Assess the morphology of the erythrocytes.
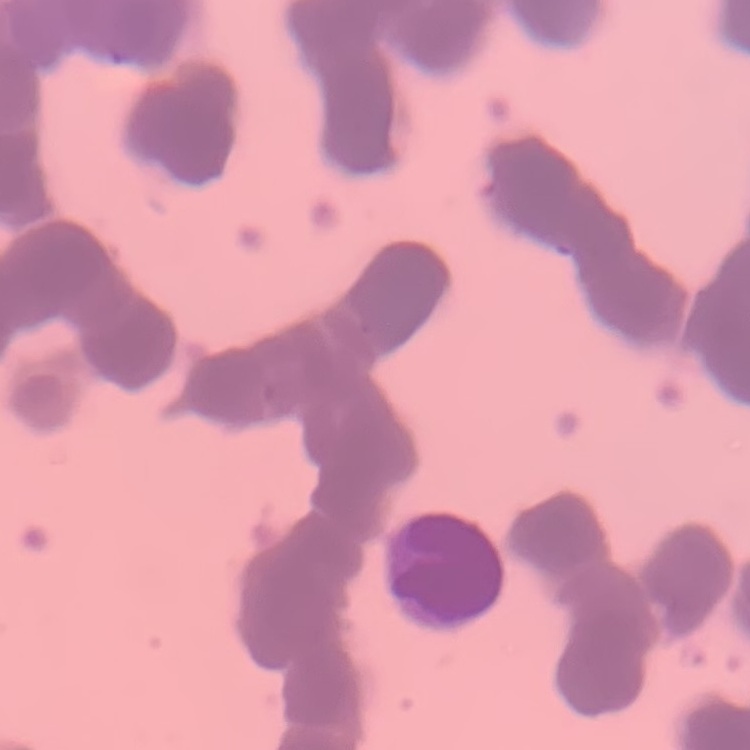
They show rouleaux formation.

Square crop of a larger photomicrograph. Thin peripheral smear. Field's or Giemsa stain.